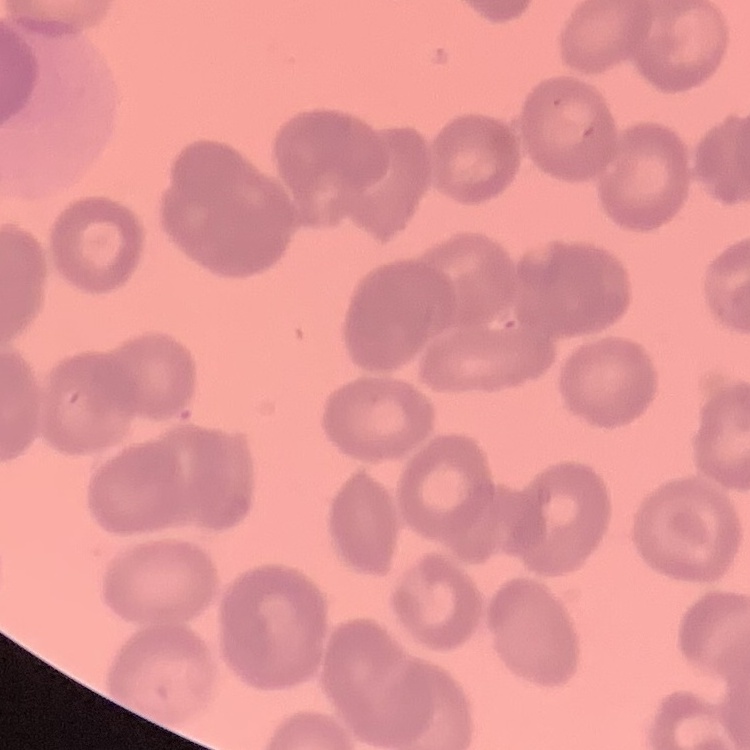 The erythrocytes exhibit rouleaux formation. Thin peripheral smear. Field's or Giemsa stain. Square crop of a larger photomicrograph.